Report the malaria status of this cell.
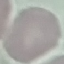
It is uninfected.

Giemsa-stained preparation. Thin smear of blood. Cell patch, automatically extracted from a larger field of view and resized to 64 × 64 pixels. Acquired by smartphone through the microscope eyepiece.